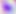 400x magnification. Toxoplasma gondii is seen. Photomicrograph.